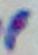
Summary:
  - Modality: photomicrograph
  - Identification: Toxoplasma gondii
  - Magnification: 1000x